Classify this cell by malaria status.
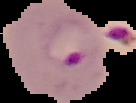

Parasitized.

Summary:
  - Image size: 136×103 pixels
  - Preparation: thin blood film
  - Image type: cell region segmented out of the field of view; surrounding area masked to black